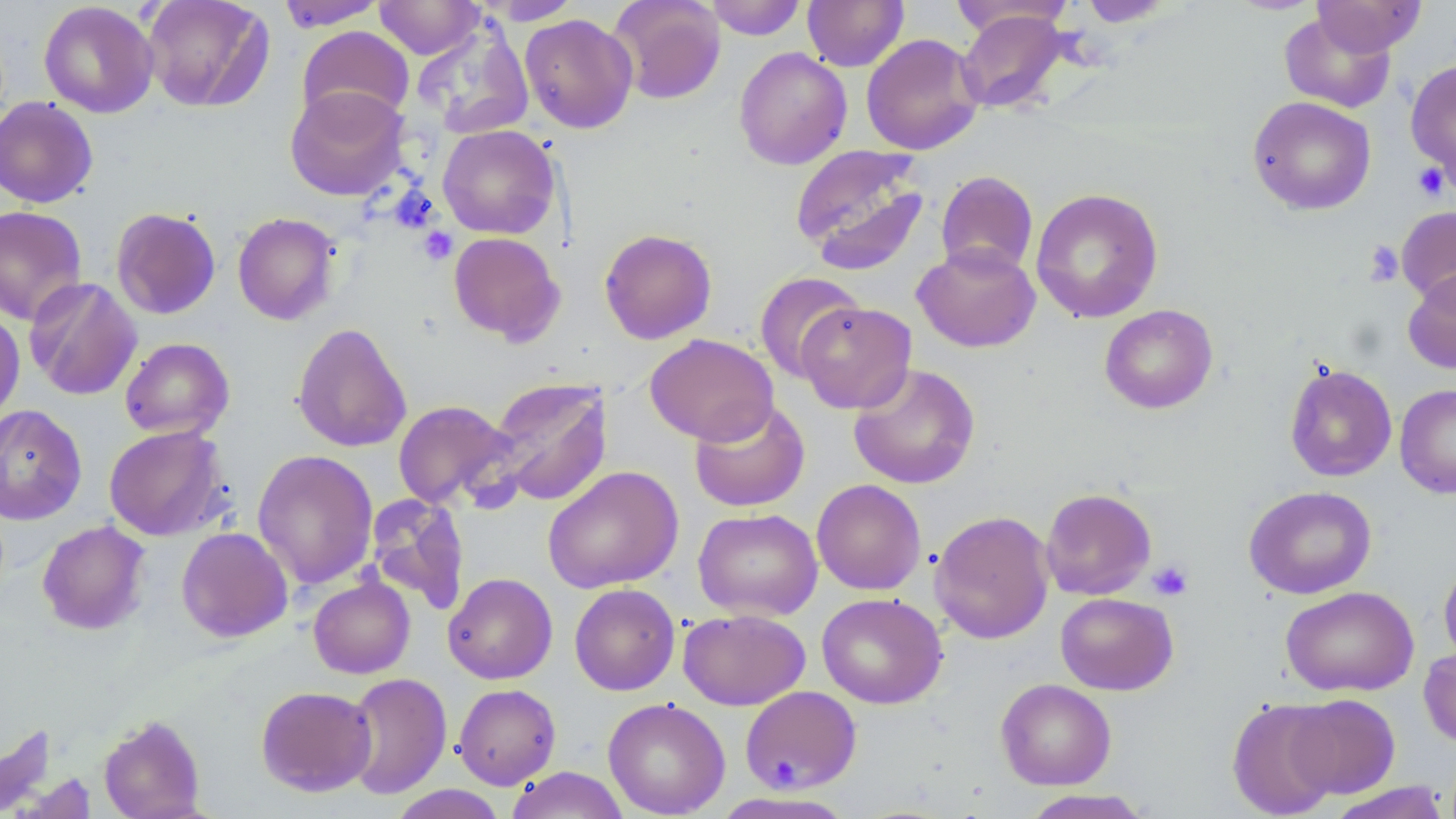
Approximate bounding boxes as (x1,y1)-(x2,y2) corner pairs in pixels. Platelet locations: (1412,162)-(1451,201), (389,186)-(439,234), (418,227)-(458,265), (1364,240)-(1404,286), (1148,559)-(1193,601). Uninfected red blood cell locations: (142,0)-(274,112), (374,0)-(484,59), (482,0)-(583,24), (608,0)-(727,105), (704,0)-(807,40), (802,0)-(908,72), (1076,0)-(1177,27), (1225,0)-(1325,15), (1312,0)-(1426,56), (39,1)-(158,118), (275,1)-(386,31), (949,1)-(1076,39), (956,8)-(1071,113), (1279,13)-(1396,113), (519,14)-(638,133), (413,20)-(534,138), (297,26)-(415,126), (861,33)-(984,155), (733,47)-(852,170), (1405,59)-(1456,188), (285,85)-(410,201), (0,96)-(99,208), (1248,96)-(1376,215), (437,124)-(561,239), (790,144)-(929,274), (935,170)-(1038,277), (1030,187)-(1164,324), (0,205)-(88,326), (1396,206)-(1456,307), (111,207)-(221,319), (232,212)-(341,325), (599,228)-(717,344), (448,232)-(564,344), (912,243)-(1040,353), (1403,268)-(1456,375), (754,271)-(866,382), (24,276)-(142,400), (795,301)-(916,414), (1100,304)-(1218,414), (0,309)-(25,424), (292,322)-(412,453), (645,333)-(778,445), (120,337)-(235,439), (848,362)-(980,490), (1284,363)-(1397,482), (484,377)-(614,508), (1394,383)-(1456,498), (689,398)-(810,512), (392,400)-(517,511), (0,404)-(87,525), (103,425)-(228,541), (252,449)-(379,589), (542,465)-(683,594), (812,479)-(926,595), (1244,485)-(1376,599), (1041,488)-(1156,600), (365,494)-(471,615), (693,508)-(823,621), (930,510)-(1054,644), (36,520)-(151,635), (176,527)-(293,642), (1438,558)-(1456,669), (443,572)-(557,684), (308,574)-(415,678), (569,583)-(680,695), (1280,585)-(1419,697), (817,592)-(947,709), (1055,593)-(1178,695), (678,608)-(810,710), (1418,645)-(1456,748), (344,672)-(453,799), (995,678)-(1116,790), (453,683)-(561,789), (256,685)-(377,796), (739,686)-(862,793), (1287,693)-(1400,799), (603,697)-(730,818), (1227,698)-(1340,817), (98,714)-(206,819), (506,766)-(630,819), (1326,782)-(1450,819), (387,785)-(509,818), (1019,789)-(1154,818). Slide-level diagnosis: negative for blood parasites. Image is 1456×819 pixels. May-Grünwald-Giemsa stain. Optical microscopy. One field of a larger specimen. Thin blood film. Captured at 1000x magnification.